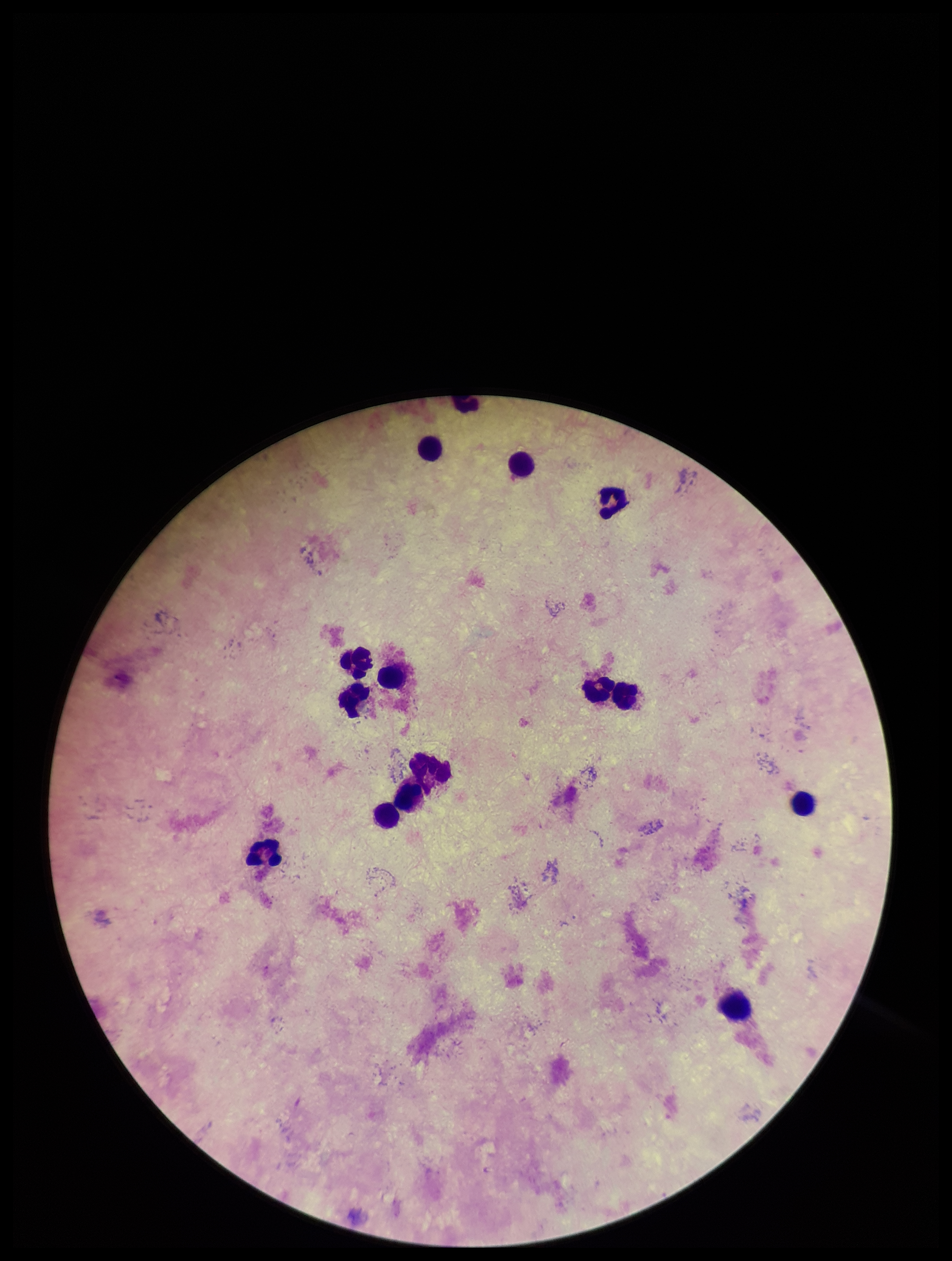
Summary:
  - Plasmodium parasites: none seen
  - Patient malaria status: negative
  - Image size: 952×1261 pixels
  - Preparation: thick smear
  - Field of view: one from this slide
  - Capture: smartphone photograph through the microscope eyepiece
  - Parasite count: 0
  - Leukocyte count: 14
  - Stain: Giemsa